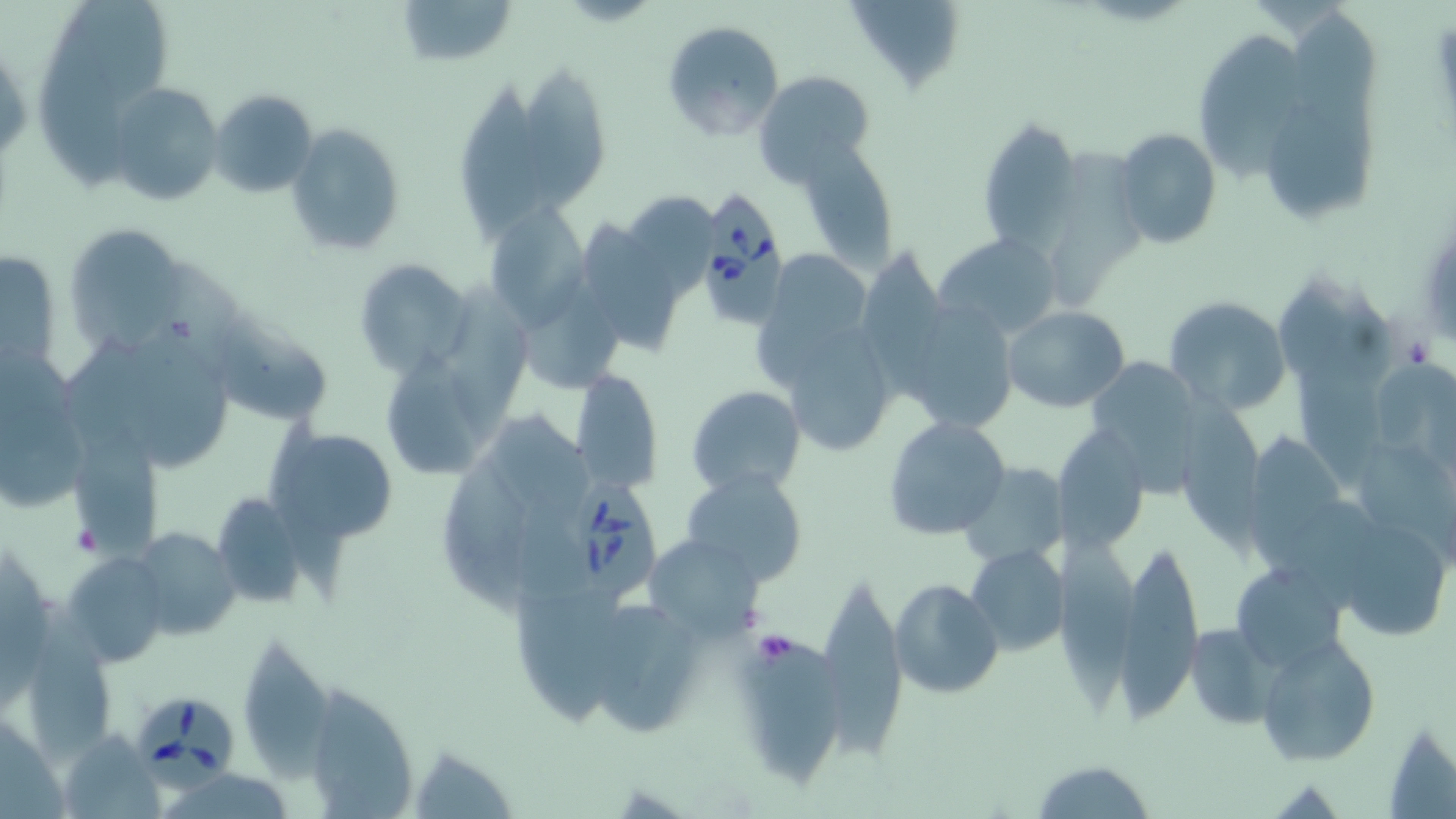

Summary:
  - Coordinate format: approximate bounding boxes as named x1/y1/x2/y2 corners in pixels
  - Platelet locations: (x1=69, y1=522, x2=105, y2=557), (x1=751, y1=631, x2=799, y2=667)
  - Babesia divergens-infected red blood cell locations: (x1=693, y1=189, x2=789, y2=329), (x1=569, y1=475, x2=668, y2=609), (x1=136, y1=690, x2=244, y2=793)
  - Uninfected red blood cell locations: (x1=396, y1=0, x2=518, y2=68), (x1=847, y1=3, x2=968, y2=96), (x1=661, y1=20, x2=785, y2=141), (x1=1193, y1=36, x2=1316, y2=182), (x1=519, y1=66, x2=612, y2=218), (x1=755, y1=72, x2=875, y2=187), (x1=458, y1=82, x2=544, y2=243), (x1=109, y1=83, x2=225, y2=206), (x1=211, y1=87, x2=319, y2=196), (x1=1267, y1=96, x2=1382, y2=225), (x1=976, y1=115, x2=1083, y2=252), (x1=285, y1=123, x2=407, y2=257), (x1=1113, y1=127, x2=1222, y2=249), (x1=795, y1=140, x2=896, y2=265), (x1=620, y1=184, x2=712, y2=301), (x1=484, y1=203, x2=590, y2=330), (x1=584, y1=222, x2=676, y2=355), (x1=65, y1=224, x2=187, y2=353), (x1=934, y1=234, x2=1062, y2=340), (x1=0, y1=245, x2=65, y2=377), (x1=861, y1=246, x2=959, y2=391), (x1=756, y1=250, x2=881, y2=386), (x1=145, y1=254, x2=260, y2=384), (x1=355, y1=256, x2=470, y2=374), (x1=439, y1=273, x2=542, y2=435), (x1=1277, y1=273, x2=1400, y2=386), (x1=1163, y1=297, x2=1291, y2=417), (x1=900, y1=299, x2=1021, y2=434), (x1=1003, y1=307, x2=1130, y2=413), (x1=213, y1=309, x2=336, y2=423), (x1=787, y1=328, x2=898, y2=452), (x1=0, y1=348, x2=91, y2=508), (x1=382, y1=354, x2=488, y2=476), (x1=1087, y1=354, x2=1215, y2=498), (x1=1295, y1=355, x2=1390, y2=490), (x1=570, y1=369, x2=664, y2=493), (x1=687, y1=385, x2=807, y2=497), (x1=1178, y1=394, x2=1264, y2=560), (x1=883, y1=415, x2=1011, y2=541), (x1=268, y1=424, x2=399, y2=543), (x1=1053, y1=426, x2=1148, y2=556), (x1=1244, y1=429, x2=1353, y2=580), (x1=67, y1=433, x2=162, y2=558), (x1=445, y1=457, x2=543, y2=626), (x1=958, y1=462, x2=1068, y2=567), (x1=681, y1=470, x2=810, y2=589), (x1=211, y1=490, x2=308, y2=607), (x1=1331, y1=515, x2=1454, y2=643), (x1=129, y1=526, x2=243, y2=642), (x1=1054, y1=532, x2=1131, y2=717), (x1=1115, y1=534, x2=1203, y2=715), (x1=642, y1=535, x2=764, y2=638), (x1=964, y1=544, x2=1069, y2=658), (x1=64, y1=551, x2=172, y2=663), (x1=1239, y1=568, x2=1358, y2=671), (x1=890, y1=580, x2=1003, y2=699), (x1=816, y1=581, x2=913, y2=760), (x1=28, y1=606, x2=119, y2=766), (x1=592, y1=614, x2=705, y2=734), (x1=1183, y1=621, x2=1279, y2=730), (x1=1258, y1=635, x2=1380, y2=767), (x1=733, y1=638, x2=844, y2=787), (x1=244, y1=641, x2=340, y2=782), (x1=311, y1=683, x2=416, y2=818), (x1=1384, y1=718, x2=1456, y2=817), (x1=58, y1=728, x2=167, y2=818), (x1=412, y1=748, x2=517, y2=819), (x1=1030, y1=758, x2=1156, y2=819)
  - Slide-level diagnosis: Babesia divergens
  - Magnification: 1000x
  - Stain: May-Grünwald-Giemsa
  - Preparation: thin blood film
  - Modality: optical microscopy
  - Field of view: single
  - Image size: 1456×819 pixels